Identify the cell.
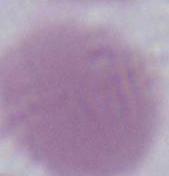

This is an erythrocyte.

modality = micrograph
magnification = 1000x